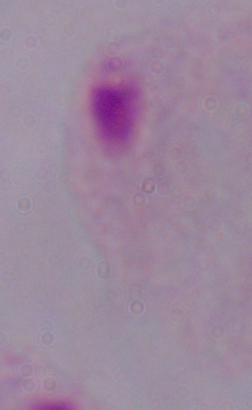
identification = trichomonad
magnification = 1000x
modality = micrograph